Classify this cell by malaria status.
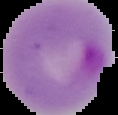

It is parasitized.

Summary:
  - Preparation: thin blood smear
  - Image type: segmented cell region on a black background
  - Image size: 118×115 pixels